Identify the parasite.
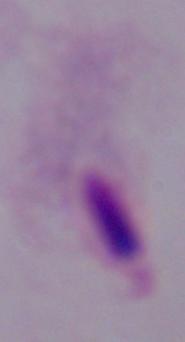
This is a trichomonad.

{
  "modality": "micrograph",
  "magnification": "1000x"
}